Report the malaria status of this cell.
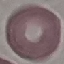
Uninfected.

Summary:
  - Capture: smartphone through the microscope eyepiece
  - Stain: Giemsa
  - Preparation: thin blood film
  - Image type: cell patch, automatically extracted from a larger field of view and resized to 64 × 64 pixels